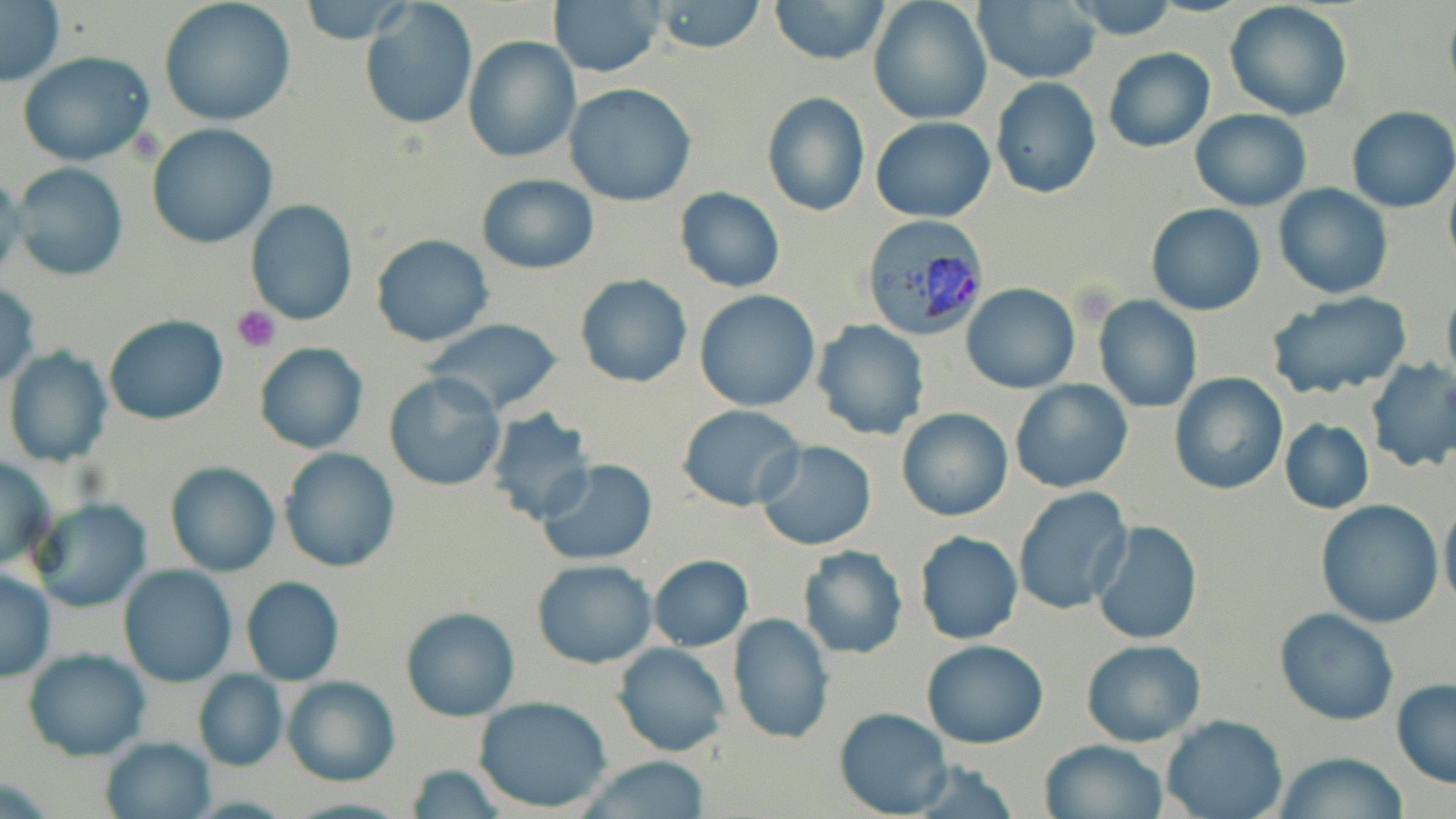

slide-level diagnosis = Plasmodium vivax
modality = light microscopy
Plasmodium vivax-infected red blood cell locations = approximate bounding boxes as [x1, y1, x2, y2] in pixels: [860, 217, 991, 341]
preparation = thin blood film
image size = 1456×819 pixels
platelet locations = approximate bounding boxes as [x1, y1, x2, y2] in pixels: [233, 306, 280, 352]
uninfected red blood cell locations = approximate bounding boxes as [x1, y1, x2, y2] in pixels: [650, 0, 768, 54], [769, 0, 891, 66], [868, 0, 992, 126], [1064, 0, 1180, 39], [0, 1, 64, 86], [157, 1, 297, 126], [299, 1, 410, 45], [548, 1, 666, 78], [1224, 1, 1353, 121], [360, 2, 478, 131], [972, 2, 1100, 83], [462, 36, 579, 161], [1103, 47, 1215, 152], [18, 53, 156, 167], [990, 77, 1102, 200], [564, 83, 696, 206], [762, 92, 869, 216], [1346, 106, 1456, 214], [1190, 108, 1310, 212], [870, 116, 995, 222], [146, 123, 278, 249], [8, 162, 129, 282], [0, 171, 27, 284], [1443, 172, 1456, 272], [476, 175, 598, 272], [1273, 184, 1393, 299], [676, 188, 785, 292], [245, 200, 357, 324], [1146, 202, 1266, 316], [370, 235, 492, 347], [574, 274, 692, 387], [0, 281, 41, 389], [962, 284, 1078, 394], [1441, 287, 1456, 390], [694, 290, 821, 410], [1264, 291, 1413, 399], [1093, 296, 1203, 414], [103, 314, 228, 425], [420, 319, 565, 418], [810, 321, 930, 440], [254, 342, 370, 453], [3, 347, 113, 467], [1366, 358, 1456, 473], [383, 372, 505, 491], [1167, 372, 1288, 496], [1011, 379, 1132, 494], [678, 404, 805, 512], [896, 408, 1014, 521], [484, 410, 594, 523], [1280, 418, 1375, 514], [754, 439, 878, 551], [278, 448, 400, 572], [0, 456, 55, 571], [537, 459, 657, 566], [164, 462, 281, 577], [1012, 488, 1133, 614], [1440, 496, 1456, 611], [30, 498, 151, 612], [1315, 500, 1444, 627], [1091, 520, 1203, 646], [914, 531, 1024, 645], [797, 546, 909, 659], [648, 554, 753, 652], [532, 560, 657, 667], [118, 564, 236, 686], [0, 567, 56, 683], [241, 576, 344, 686], [401, 607, 519, 721], [1274, 608, 1399, 725], [727, 614, 833, 745], [1081, 639, 1205, 748], [921, 640, 1049, 749], [613, 641, 732, 756], [23, 647, 151, 761], [192, 668, 287, 770], [282, 675, 399, 785], [1392, 680, 1456, 788], [473, 697, 612, 814], [835, 707, 952, 817], [1162, 715, 1288, 819], [101, 735, 214, 818], [1040, 738, 1167, 819], [1272, 752, 1408, 819], [575, 758, 715, 817], [902, 760, 1024, 819], [403, 764, 507, 819]
stain = May-Grünwald-Giemsa
magnification = 1000x
field of view = single